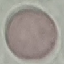
{
  "malaria_status": "uninfected",
  "stain": "Giemsa",
  "preparation": "thin blood smear",
  "capture": "smartphone through the microscope eyepiece",
  "image_type": "automatically extracted cell patch, resized to 64 × 64 pixels"
}